Locate every blood parasite and identify its species.
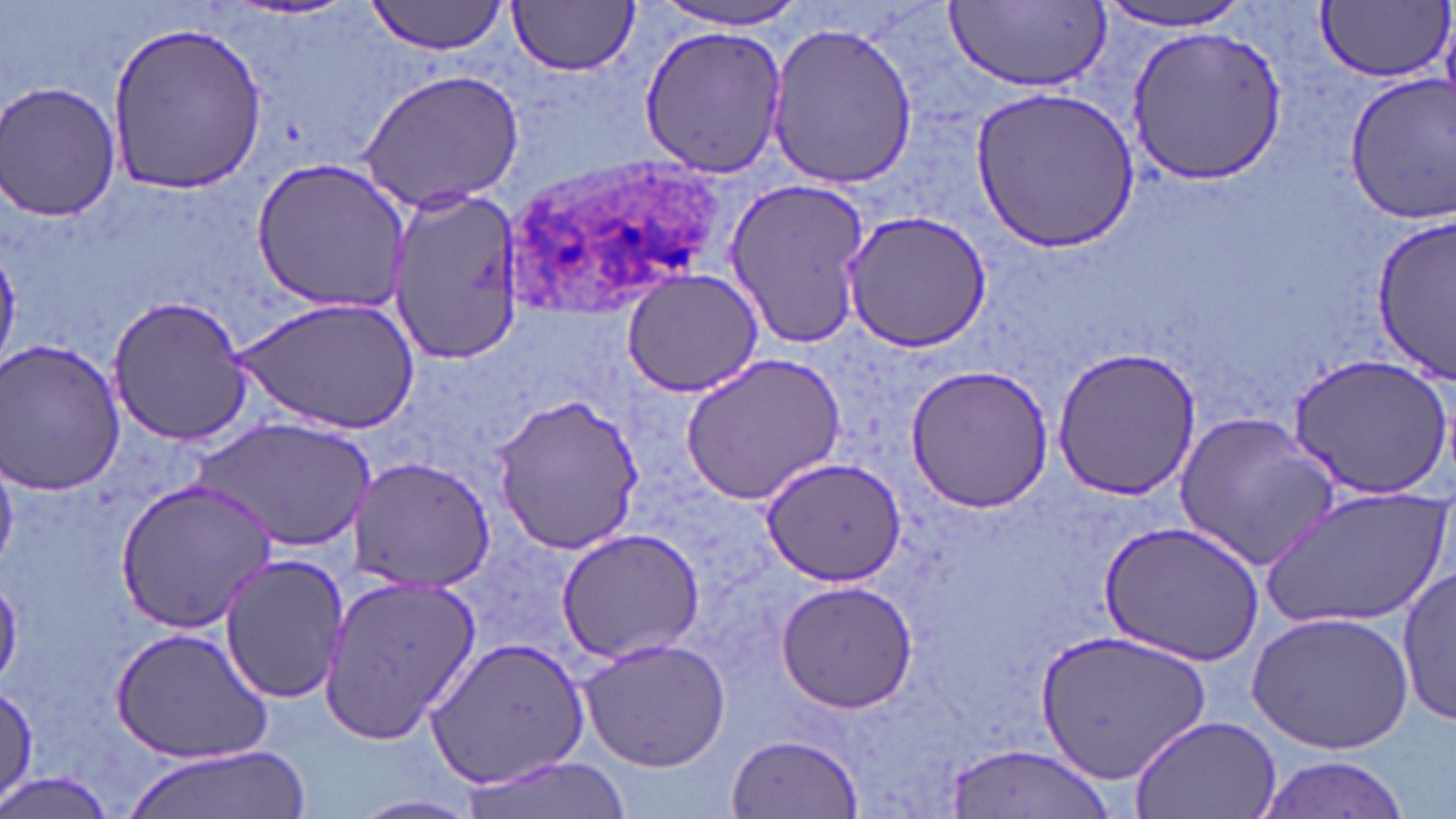
Approximate bounding boxes as (x1, y1, x2, y2) in pixels.
Plasmodium ovale-infected red blood cells: (501, 156, 731, 316).
No Plasmodium falciparum, Plasmodium malariae, Plasmodium vivax, Babesia divergens, or Trypanosoma brucei observed.

slide-level diagnosis = Plasmodium ovale
magnification = 1000x
stain = May-Grünwald-Giemsa
image size = 1456×819 pixels
modality = light microscopy
uninfected red blood cell locations = approximate bounding boxes as (x1, y1, x2, y2) in pixels: (365, 0, 512, 57), (652, 0, 813, 30), (508, 1, 641, 76), (945, 2, 1111, 90), (1317, 2, 1450, 83), (1096, 3, 1258, 33), (107, 18, 268, 193), (765, 20, 919, 190), (639, 24, 787, 178), (1124, 24, 1287, 184), (356, 69, 526, 213), (1342, 70, 1455, 225), (2, 81, 121, 223), (970, 85, 1138, 254), (249, 158, 412, 313), (723, 178, 872, 350), (390, 188, 520, 367), (841, 209, 994, 352), (1373, 214, 1456, 380), (619, 267, 767, 398), (107, 295, 256, 448), (233, 296, 421, 436), (0, 338, 128, 496), (1050, 343, 1201, 502), (678, 351, 848, 507), (1287, 352, 1453, 500), (903, 364, 1057, 514), (491, 393, 646, 555), (1173, 412, 1340, 571), (196, 419, 374, 552), (348, 454, 495, 593), (760, 457, 906, 589), (114, 477, 277, 632), (1264, 481, 1448, 630), (1098, 520, 1264, 666), (555, 527, 705, 665), (219, 553, 349, 705), (1398, 567, 1454, 728), (318, 573, 480, 746), (775, 580, 918, 713), (1248, 611, 1415, 754), (110, 626, 273, 763), (1037, 627, 1212, 788), (426, 635, 589, 790), (579, 637, 730, 772), (1, 681, 39, 806), (1127, 714, 1282, 818), (727, 733, 863, 817), (124, 743, 309, 819), (945, 744, 1113, 817), (1256, 754, 1411, 818), (456, 757, 630, 819), (0, 771, 118, 819), (350, 795, 484, 819)
preparation = thin blood smear
field of view = one of a larger specimen